Assess the morphology of the red blood cells.
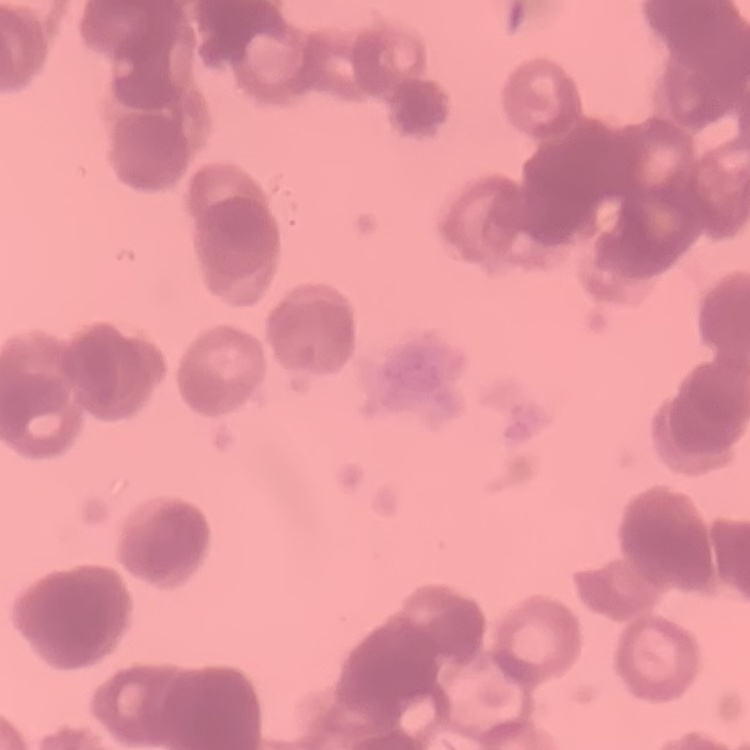
Rouleaux formation.

Thin blood smear. One tile cut from a larger photomicrograph. Stained with either Field's or Giemsa.